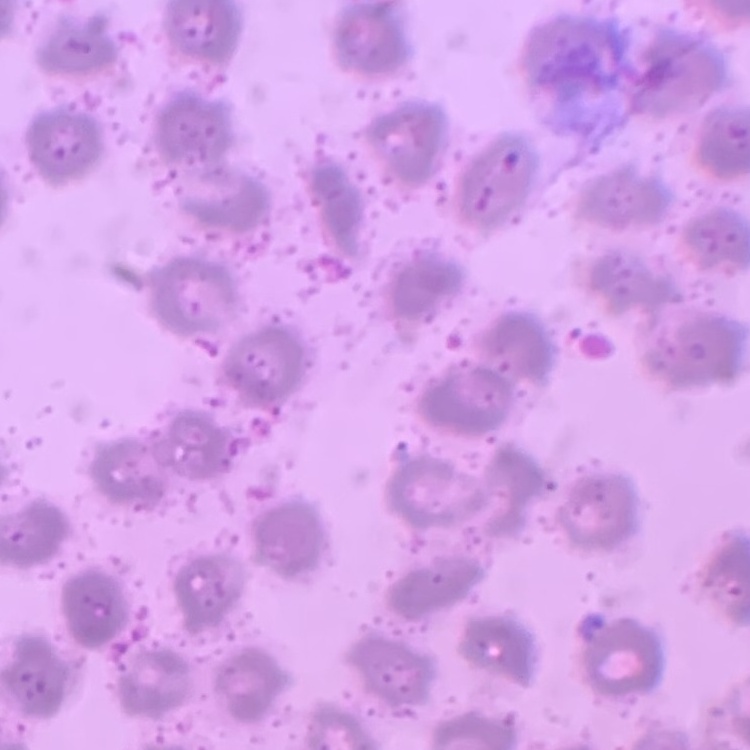 The red blood cells exhibit no rouleaux formation. Thin blood smear. One tile cut from a larger photomicrograph. Field's or Giemsa stain.